Name the blood parasite species.
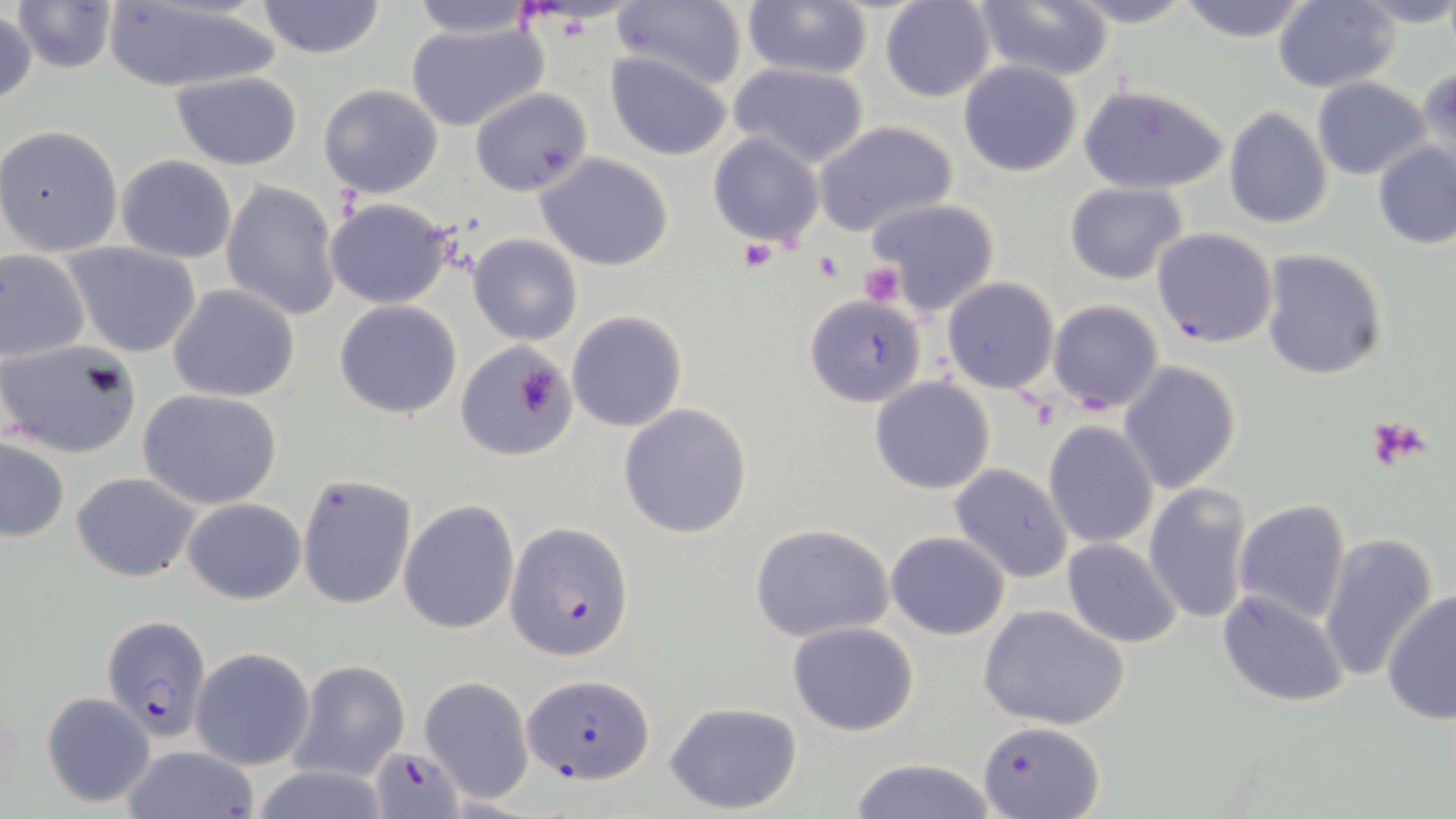
Plasmodium falciparum.

field_of_view: single
plasmodium_falciparum_infected_red_blood_cell_locations: 'approximate bounding boxes as (x1,y1)-(x2,y2) corner pairs in pixels: (1150,227)-(1277,348), (505,523)-(634,660), (101,614)-(212,741), (524,673)-(653,784), (978,716)-(1104,816), (370,746)-(465,818)'
preparation: thin blood smear
modality: light microscopy
stain: May-Grünwald-Giemsa
uninfected_red_blood_cell_locations: 'approximate bounding boxes as (x1,y1)-(x2,y2) corner pairs in pixels: (404,0)-(541,41), (610,0)-(749,91), (740,0)-(874,81), (1062,0)-(1201,28), (1271,0)-(1400,92), (10,1)-(123,75), (102,1)-(281,92), (254,1)-(387,59), (879,1)-(996,103), (968,1)-(1112,81), (1174,1)-(1316,45), (1353,1)-(1456,29), (0,9)-(37,107), (403,17)-(553,134), (605,51)-(731,160), (958,60)-(1082,176), (725,61)-(873,168), (1415,66)-(1456,177), (169,71)-(303,169), (1310,77)-(1432,180), (318,84)-(445,198), (1077,84)-(1229,196), (469,88)-(593,197), (1224,106)-(1333,229), (813,121)-(959,239), (0,125)-(124,258), (708,133)-(825,247), (1372,142)-(1456,250), (535,154)-(675,272), (115,156)-(236,264), (220,180)-(342,322), (1064,181)-(1189,285), (323,197)-(456,308), (863,198)-(1002,318), (467,234)-(582,345), (62,242)-(201,357), (1,248)-(90,363), (1259,248)-(1389,380), (942,278)-(1059,393), (168,283)-(301,402), (803,293)-(924,408), (334,300)-(463,419), (1047,300)-(1164,414), (567,311)-(689,432), (0,339)-(140,458), (455,341)-(578,461), (1119,361)-(1242,494), (870,377)-(996,494), (138,388)-(283,509), (617,402)-(753,539), (1043,420)-(1159,550), (0,439)-(70,542), (949,463)-(1074,583), (71,471)-(200,582), (295,474)-(415,611), (1143,481)-(1254,626), (183,498)-(306,604), (1231,498)-(1351,625), (399,499)-(520,634), (750,523)-(896,644), (886,531)-(1011,641), (1318,533)-(1438,683), (1062,540)-(1183,648), (1380,588)-(1455,726), (1216,589)-(1349,707), (977,603)-(1130,731), (788,621)-(920,736), (190,646)-(315,770), (289,661)-(410,782), (420,674)-(535,803), (41,693)-(156,807), (663,701)-(805,815), (120,745)-(260,819), (843,758)-(1003,818), (247,766)-(391,818)'
platelet_locations: 'approximate bounding boxes as (x1,y1)-(x2,y2) corner pairs in pixels: (740,240)-(777,273), (814,251)-(845,282), (858,263)-(905,307), (514,350)-(566,420), (1365,414)-(1434,472)'
image_size: 1456×819 pixels
magnification: 1000x